Assess this cell for malaria.
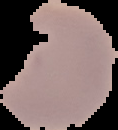
It is parasitized.

image size = 118×130 pixels
preparation = thin blood film
image type = cell region segmented out of the field of view; surrounding area masked to black